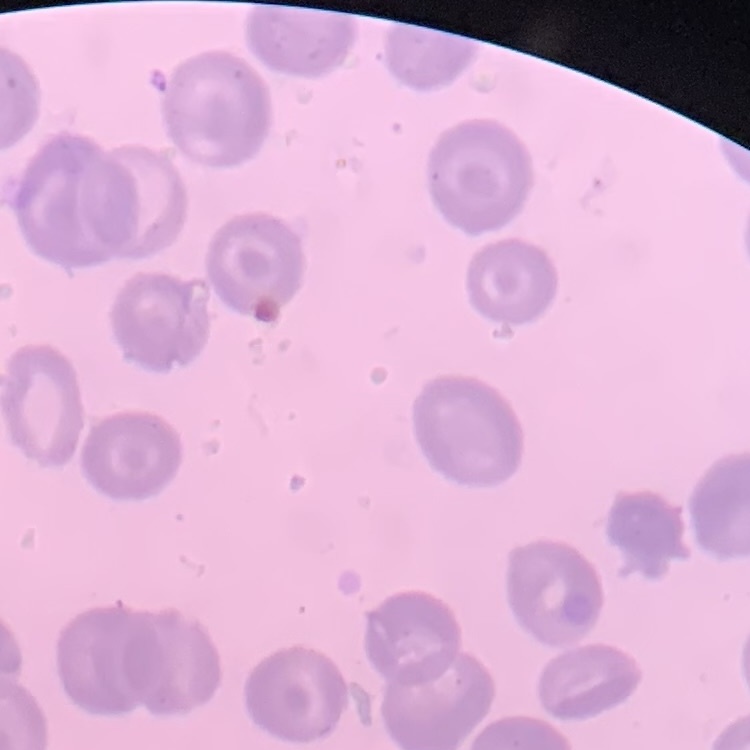

red blood cell morphology = no rouleaux formation
stain = Field's or Giemsa
preparation = thin peripheral smear
image type = square crop of a larger photomicrograph